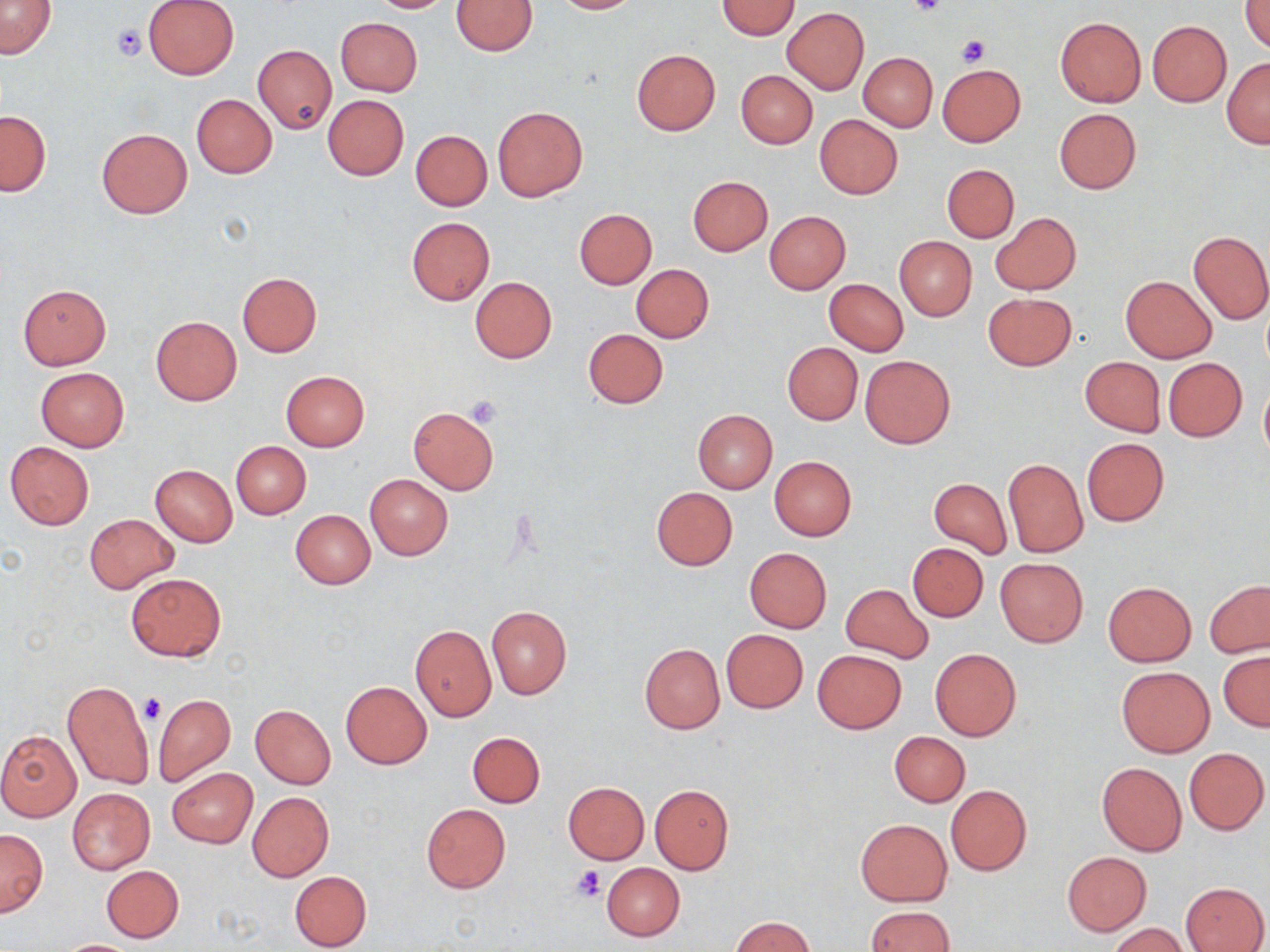
slide_level_diagnosis: no evidence of blood parasites
modality: light microscopy
preparation: thin blood film
uninfected_red_blood_cell_locations: 'approximate bounding boxes as (x1, y1, x2, y2) in pixels: (144, 0, 239, 79), (365, 0, 457, 13), (452, 0, 539, 56), (549, 0, 644, 14), (0, 1, 57, 59), (717, 1, 800, 40), (1242, 1, 1270, 51), (782, 7, 869, 94), (335, 17, 423, 96), (1055, 17, 1145, 107), (1147, 21, 1231, 106), (253, 45, 336, 133), (631, 49, 720, 135), (859, 52, 937, 131), (1221, 56, 1270, 148), (937, 64, 1025, 147), (736, 69, 818, 149), (191, 93, 277, 178), (322, 94, 410, 181), (493, 107, 588, 201), (1053, 108, 1142, 194), (0, 110, 50, 195), (814, 115, 903, 199), (97, 128, 192, 218), (410, 129, 492, 210), (943, 165, 1019, 242), (687, 176, 773, 256), (574, 209, 656, 289), (765, 212, 850, 293), (992, 212, 1081, 295), (406, 217, 494, 304), (1187, 229, 1270, 325), (894, 236, 976, 321), (631, 264, 714, 343), (236, 272, 322, 357), (1121, 275, 1217, 363), (469, 277, 556, 364), (824, 279, 909, 355), (18, 284, 111, 369), (983, 292, 1076, 371), (151, 316, 241, 405), (582, 328, 667, 409), (783, 343, 862, 424), (860, 354, 956, 449), (1080, 356, 1165, 436), (1164, 358, 1246, 440), (36, 367, 128, 451), (281, 370, 369, 451), (1259, 383, 1270, 462), (408, 406, 499, 494), (692, 408, 777, 494), (1082, 437, 1169, 525), (231, 440, 311, 519), (5, 441, 95, 530), (769, 456, 857, 541), (1004, 460, 1087, 557), (150, 464, 237, 546), (364, 474, 453, 560), (929, 478, 1011, 557), (650, 486, 737, 570), (289, 509, 376, 589), (84, 514, 178, 593), (908, 543, 988, 622), (745, 548, 831, 632), (995, 558, 1089, 647), (127, 572, 225, 661), (1205, 580, 1270, 658), (1103, 581, 1196, 666), (841, 583, 933, 663), (485, 605, 571, 700), (410, 624, 496, 720), (721, 629, 808, 712), (642, 639, 808, 722), (639, 643, 725, 734), (930, 649, 1021, 741), (813, 650, 907, 734), (1219, 652, 1269, 731), (1116, 666, 1216, 758), (61, 680, 154, 790), (340, 681, 432, 769), (153, 694, 235, 787), (250, 704, 336, 789), (0, 729, 82, 822), (890, 731, 970, 807), (466, 732, 545, 807), (1184, 748, 1269, 834), (1097, 762, 1187, 855), (166, 767, 257, 848), (563, 781, 649, 863), (650, 784, 734, 874), (945, 784, 1031, 876), (67, 787, 157, 874), (247, 792, 334, 881), (421, 803, 511, 894), (855, 817, 952, 906), (0, 828, 48, 916), (1063, 852, 1152, 935), (601, 862, 685, 940), (101, 865, 184, 942), (289, 870, 371, 951), (1181, 881, 1269, 952), (864, 907, 954, 952), (730, 916, 815, 952), (1108, 923, 1188, 952), (53, 939, 142, 951)'
stain: May-Grünwald-Giemsa
magnification: 1000x
platelet_locations: 'approximate bounding boxes as (x1, y1, x2, y2) in pixels: (909, 0, 945, 19), (111, 24, 145, 60), (956, 36, 990, 67), (465, 395, 503, 429), (140, 694, 167, 724), (570, 865, 604, 903)'
field_of_view: one of a larger specimen
image_size: 1270×952 pixels